Point out each Plasmodium parasite.
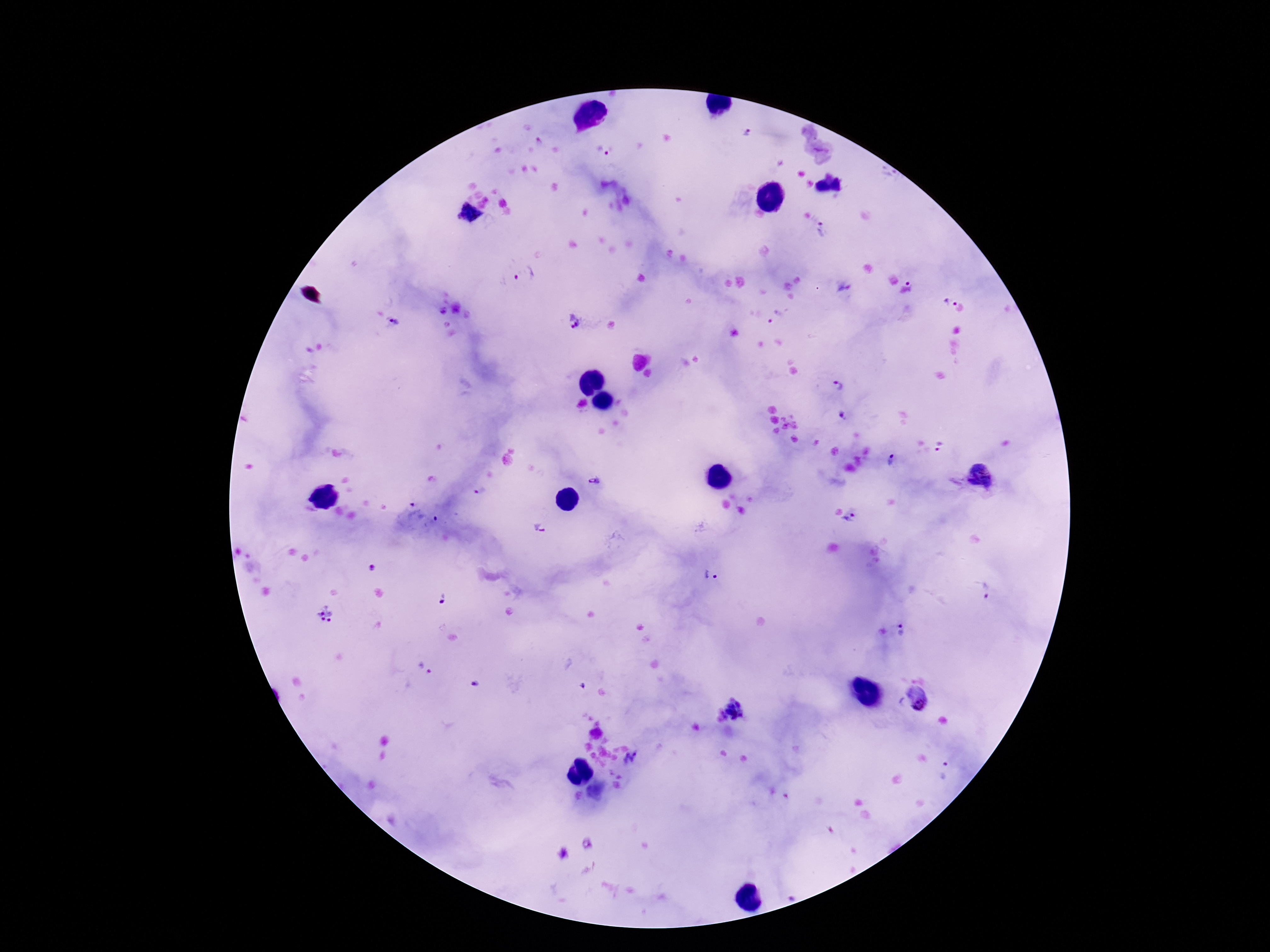
Approximate object centers, in pixels from the top-left corner.
Plasmodium parasites: (x=747, y=132), (x=601, y=151), (x=469, y=213), (x=823, y=230), (x=523, y=274), (x=910, y=280), (x=844, y=293), (x=951, y=302), (x=776, y=317), (x=572, y=323), (x=396, y=324), (x=839, y=387), (x=844, y=417), (x=939, y=447), (x=889, y=460), (x=979, y=477), (x=594, y=482), (x=481, y=493), (x=413, y=509), (x=852, y=519), (x=430, y=522), (x=540, y=530), (x=375, y=568), (x=712, y=575), (x=987, y=591), (x=440, y=599), (x=326, y=614), (x=905, y=629), (x=426, y=667), (x=474, y=684), (x=916, y=697), (x=732, y=709), (x=632, y=760), (x=946, y=770), (x=586, y=844).

patient malaria status = infected
field of view = one from this slide
stain = Giemsa
capture = smartphone camera through the microscope eyepiece
magnification = 100x
preparation = thick peripheral-blood smear
image size = 1270×952 pixels